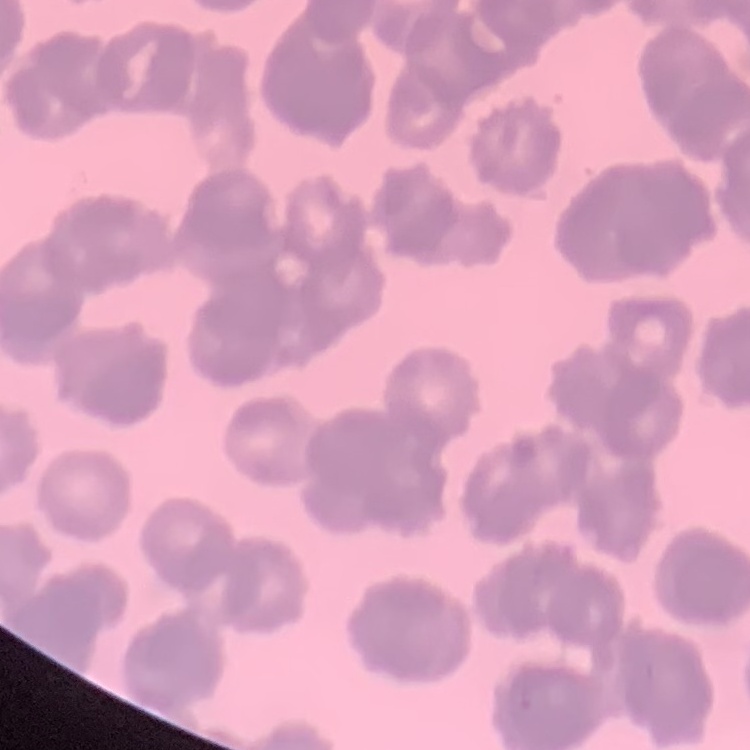
Summary:
  - Erythrocyte morphology: rouleaux formation
  - Stain: Field's or Giemsa
  - Image type: square crop of a larger photomicrograph
  - Preparation: thin peripheral smear